Name the parasite shown.
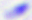

This is Toxoplasma gondii.

{
  "magnification": "400x",
  "modality": "photomicrograph"
}